Assess this cell for malaria.
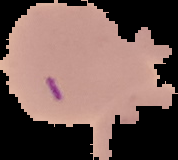
Uninfected.

image type = segmented cell region on a black background
preparation = thin blood film
image size = 178×160 pixels